Report the malaria status.
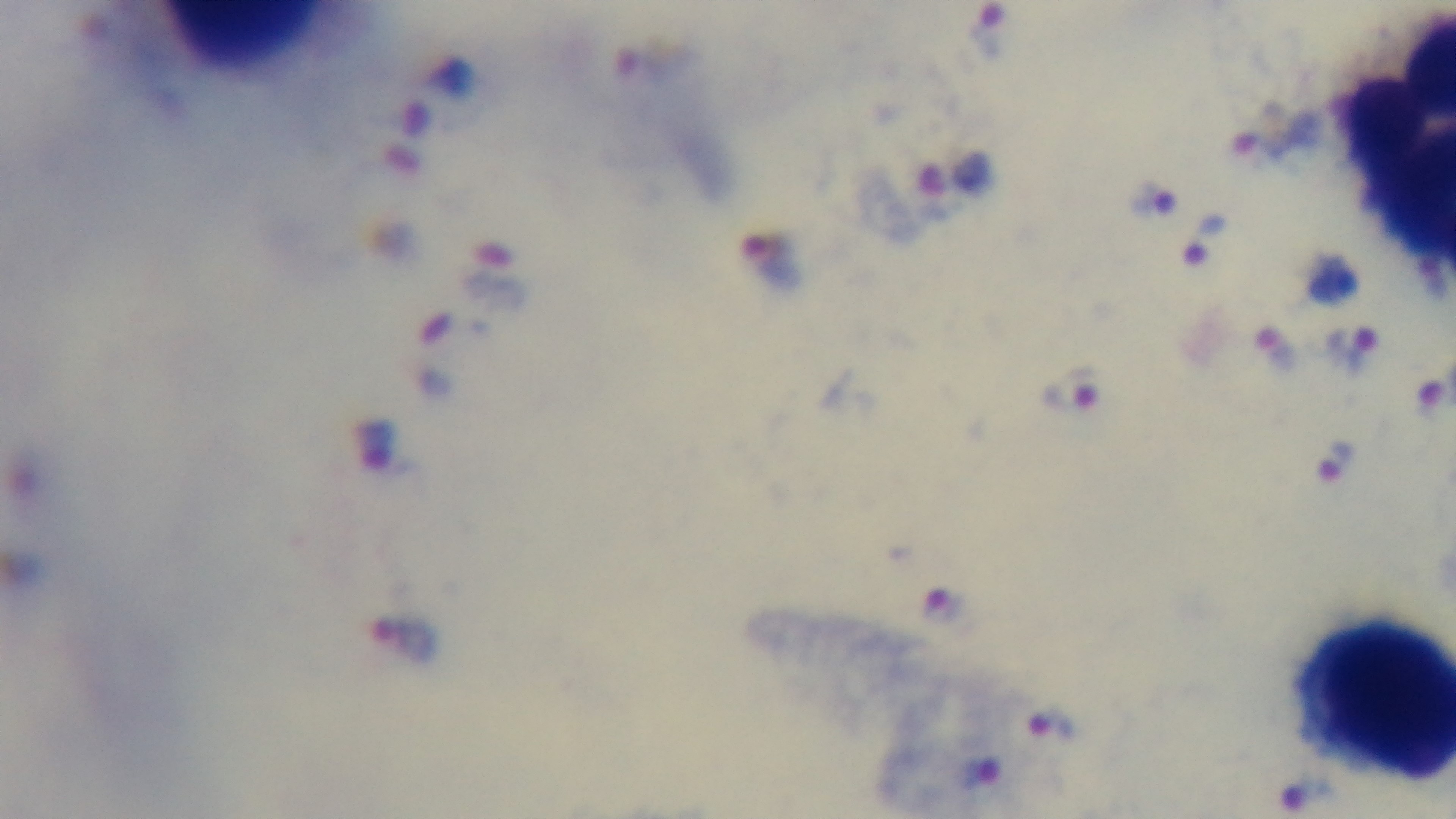
Positive.

Summary:
  - Objective: 100x oil immersion
  - Capture: mounted 4K digital camera
  - Preparation: thick blood film
  - Modality: light microscopy
  - Stain: Giemsa
  - Field of view: single